Report the malaria status of this cell.
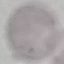
It is uninfected.

Thin blood smear. Photographed with a smartphone camera at the microscope eyepiece. Automatically extracted cell patch, resized to 64 × 64 pixels. Giemsa-stained preparation.